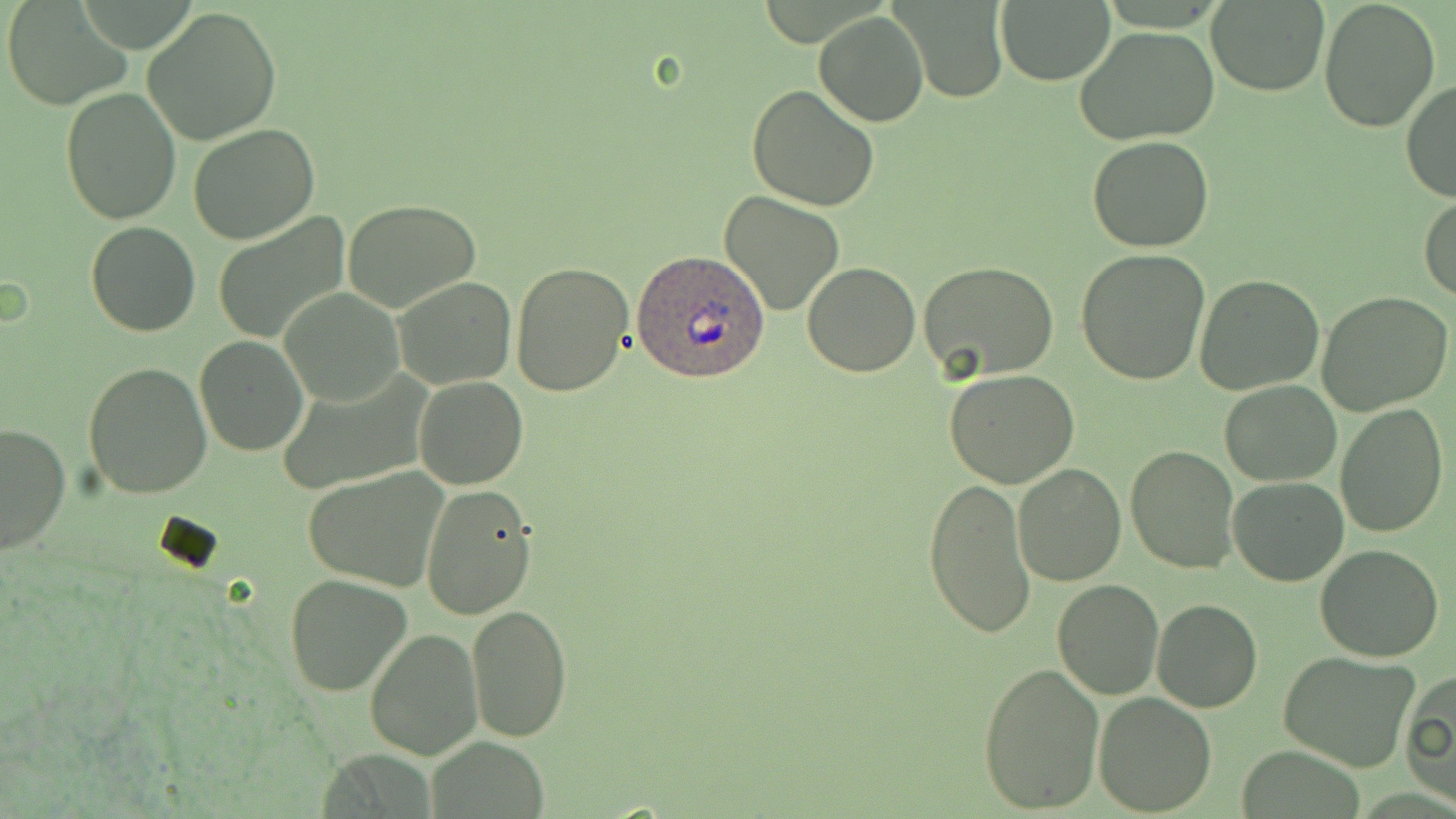
Approximate bounding boxes as (x1,y1)-(x2,y2) corner pairs in pixels. Plasmodium ovale-infected red blood cell locations: (632,249)-(770,381). Uninfected red blood cell locations: (899,0)-(1010,103), (1318,0)-(1440,133), (5,2)-(129,110), (995,2)-(1114,85), (1205,2)-(1329,95), (141,6)-(282,145), (813,9)-(928,126), (1074,26)-(1219,147), (1401,80)-(1456,205), (746,84)-(880,211), (60,87)-(182,227), (187,125)-(319,245), (1087,136)-(1213,254), (720,192)-(845,316), (1418,194)-(1456,303), (343,200)-(481,313), (212,212)-(351,344), (85,220)-(200,337), (1075,249)-(1210,384), (919,261)-(1061,385), (510,262)-(632,396), (802,262)-(920,377), (392,275)-(517,390), (1193,275)-(1324,395), (279,286)-(405,407), (1316,290)-(1452,415), (194,336)-(308,457), (83,361)-(213,498), (943,370)-(1080,490), (274,372)-(432,495), (412,375)-(527,489), (1219,381)-(1342,487), (1335,403)-(1449,538), (0,421)-(72,556), (1124,445)-(1240,575), (1011,462)-(1126,586), (304,468)-(448,592), (1228,475)-(1348,587), (922,477)-(1033,637), (420,484)-(539,620), (1313,546)-(1445,663), (284,573)-(414,697), (1051,578)-(1164,701), (1152,598)-(1262,713), (466,605)-(572,740), (365,628)-(484,760), (1277,650)-(1422,772), (976,661)-(1107,814), (1402,667)-(1456,809), (1093,689)-(1218,815), (426,739)-(549,817), (1237,744)-(1367,818). Slide-level diagnosis: Plasmodium ovale. Optical microscopy. 1000x magnification. Thin blood smear. May-Grünwald-Giemsa stain. Single field of view. Image is 1456×819 pixels.